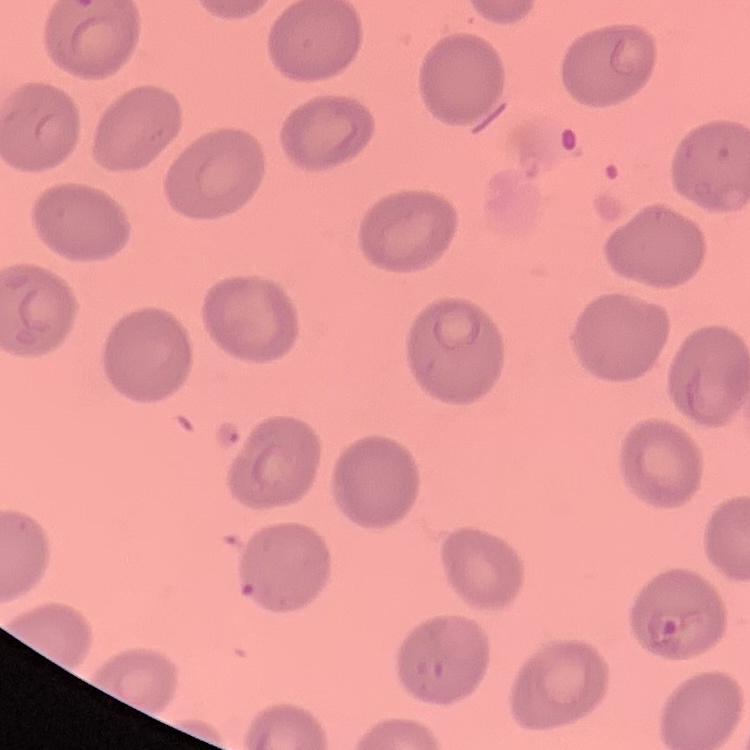
The red blood cells show no rouleaux formation. One tile cut from a larger photomicrograph. Thin blood smear. Stained with either Field's or Giemsa.